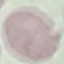

Summary:
  - Result: no malaria parasites seen
  - Image type: cell patch, automatically extracted from a larger field of view and resized to 64 × 64 pixels
  - Stain: Giemsa
  - Preparation: thin smear
  - Capture: smartphone camera at the microscope eyepiece